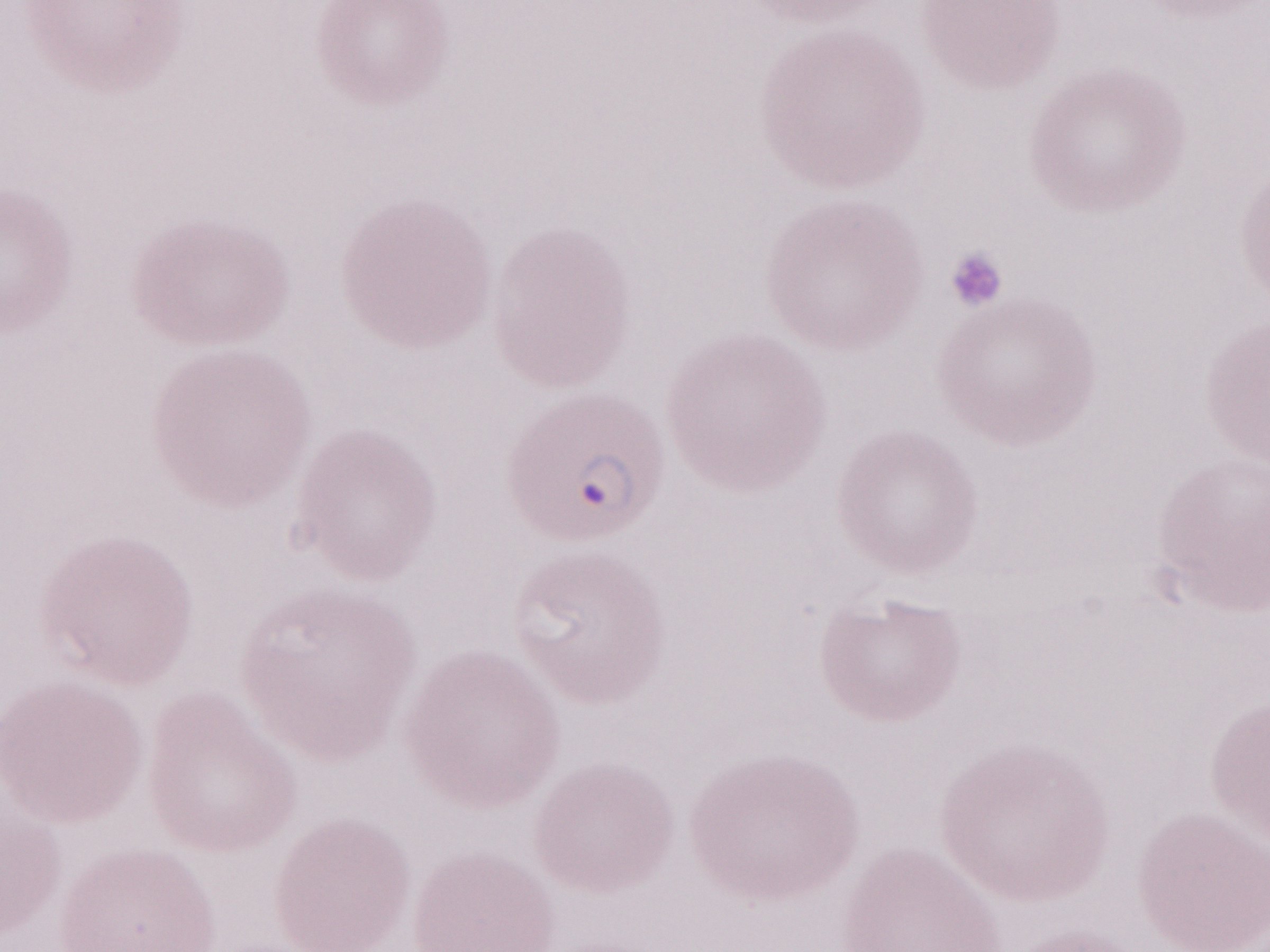 Thin blood film. Magnification: 1,000x. May-Grünwald-Giemsa-stained preparation. Patient diagnosis: malaria infection. Single field of view. Image is 1270×952 pixels. Olympus BX43 microscope, Olympus DP73 camera.